Report the malaria status.
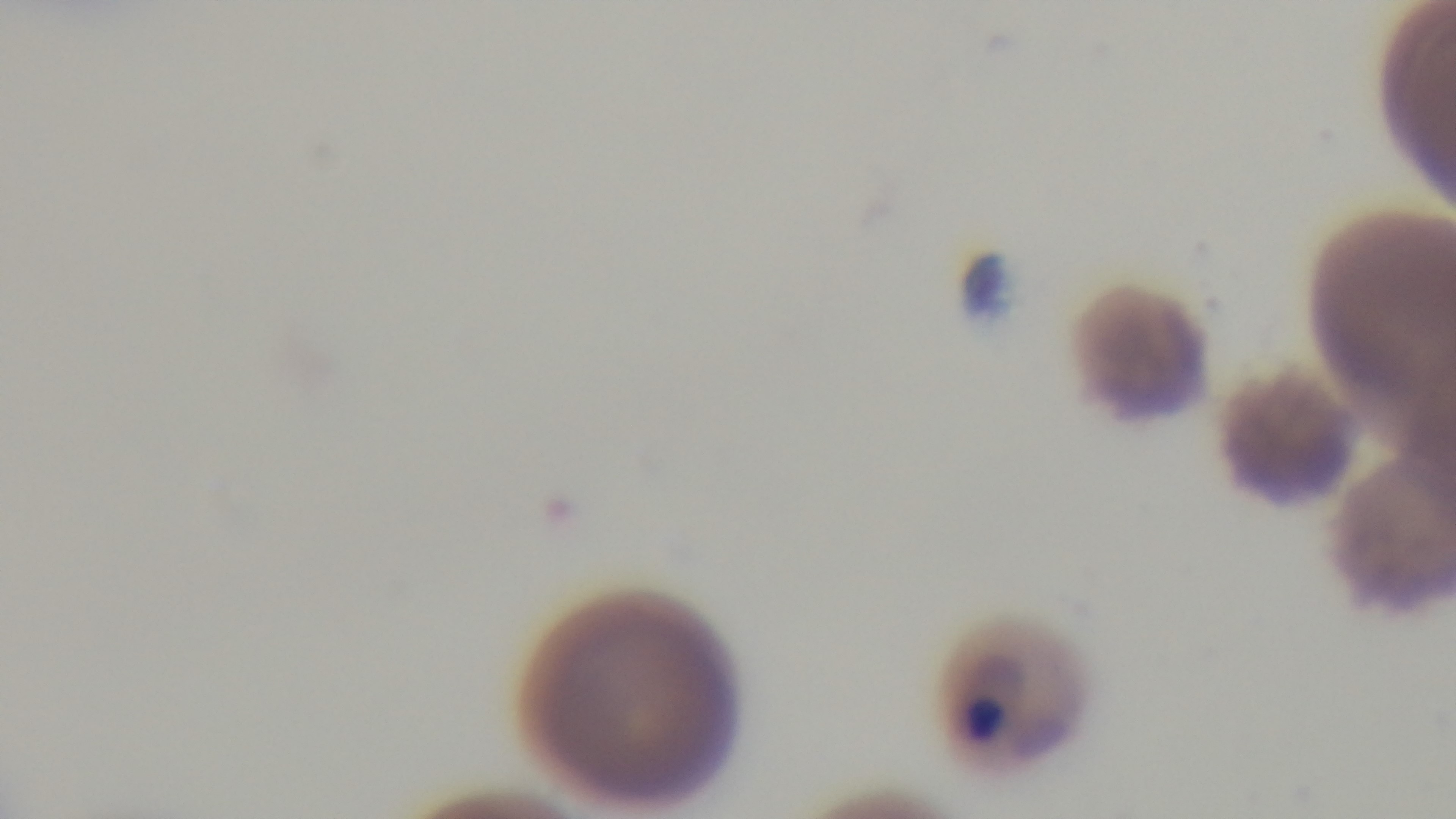

Infected.

Mounted 4K digital camera. Photomicrograph. 100x oil-immersion objective. Preparation: thin. Giemsa-stained. One field from the slide.